State which cell type is depicted.
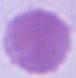
This is an erythrocyte.

Summary:
  - Modality: micrograph
  - Magnification: 1000x